Comment on the morphology of the red blood cells.
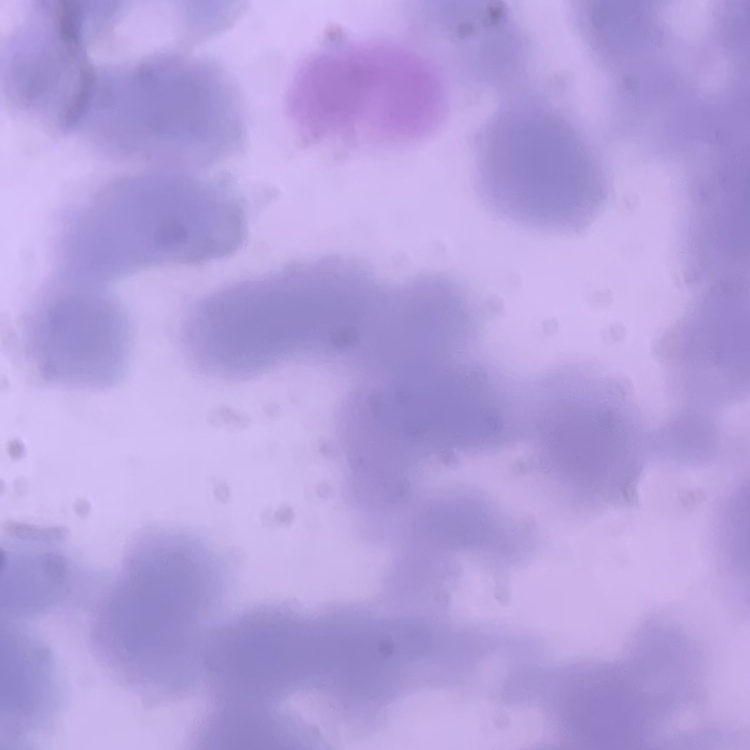
They show rouleaux formation.

Thin peripheral smear. Square crop of a larger photomicrograph. Stained with either Field's or Giemsa.